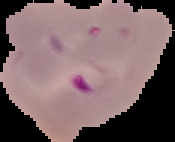

From a thin blood smear. Image is 175×142 pixels. Cell region segmented out of the field of view; the surrounding area is masked to black. Malaria status: parasitized.